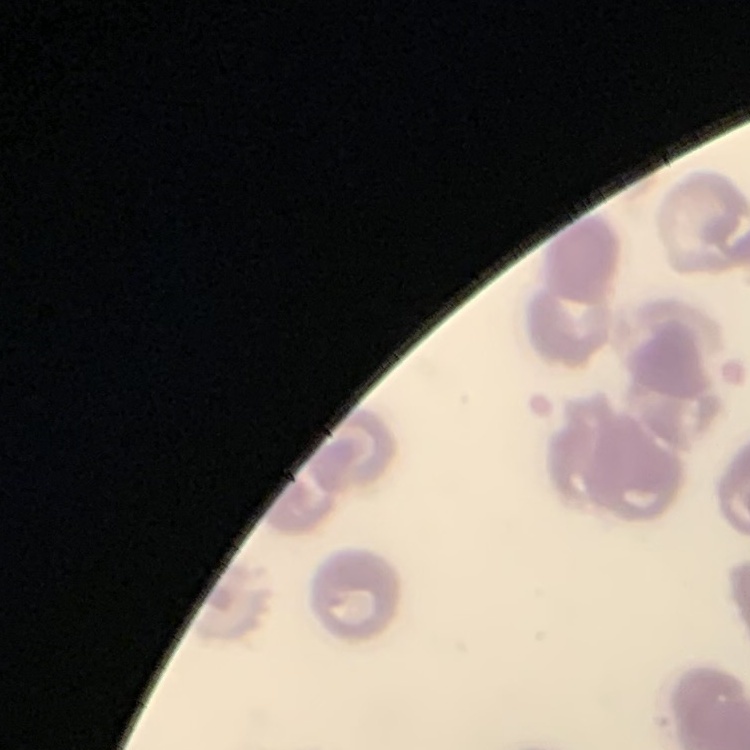 The red blood cells show no rouleaux formation. Thin blood film. Square crop of a larger photomicrograph. Stained with either Field's or Giemsa.